Assess this cell for malaria.
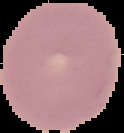
Uninfected.

Summary:
  - Image type: cell region segmented out of the field of view; surrounding area masked to black
  - Preparation: thin blood smear
  - Image size: 124×133 pixels